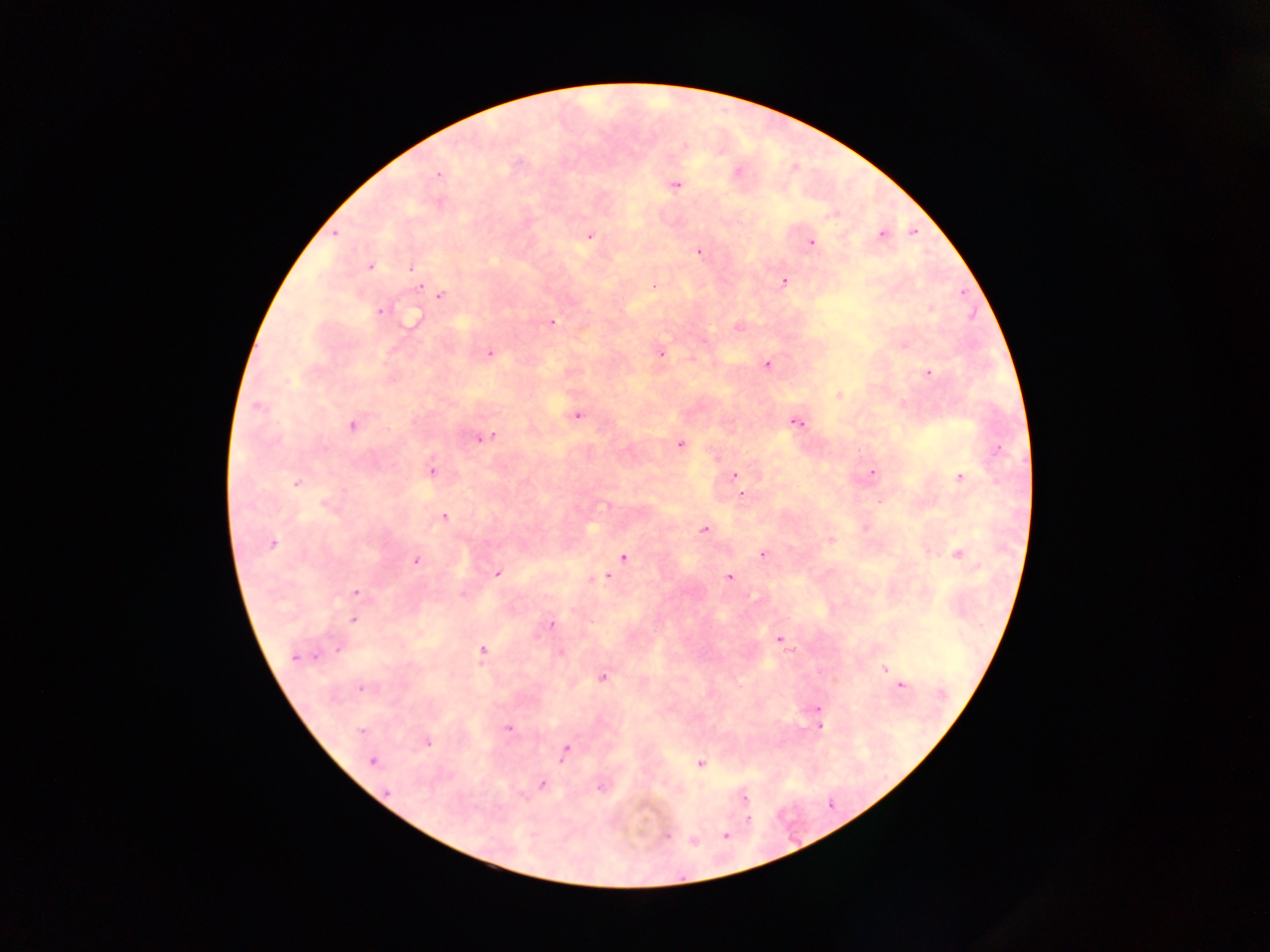
Approximate centers as [x, y] in pixels. Malaria parasite locations: [684, 145], [737, 173], [438, 175], [675, 185], [335, 233], [881, 235], [590, 236], [812, 242], [699, 252], [370, 267], [412, 268], [784, 282], [652, 286], [419, 287], [440, 295], [930, 309], [380, 310], [412, 320], [552, 322], [738, 326], [903, 345], [490, 353], [660, 353], [767, 365], [928, 373], [838, 395], [258, 406], [576, 416], [796, 422], [352, 426], [490, 436], [480, 438], [680, 445], [998, 450], [431, 470], [872, 473], [735, 475], [960, 477], [296, 483], [742, 493], [606, 505], [328, 506], [444, 516], [704, 530], [831, 540], [271, 543], [762, 554], [958, 554], [623, 557], [415, 561], [497, 574], [729, 577], [604, 578], [356, 592], [463, 595], [352, 620], [551, 625], [779, 640], [338, 649], [482, 651], [560, 652], [314, 656], [295, 657], [884, 669], [893, 676], [603, 677], [901, 685], [362, 688], [818, 708], [820, 726], [508, 728], [361, 730], [428, 742], [566, 750], [372, 761], [701, 764], [542, 784], [601, 786], [523, 795], [744, 799], [748, 819], [726, 835], [666, 836], [694, 841]. Thick blood smear. Single field of view. Image is 1270×952 pixels. Sample from Ghana. Photographed through a microscope with a mobile-phone camera.